Name the blood parasite species.
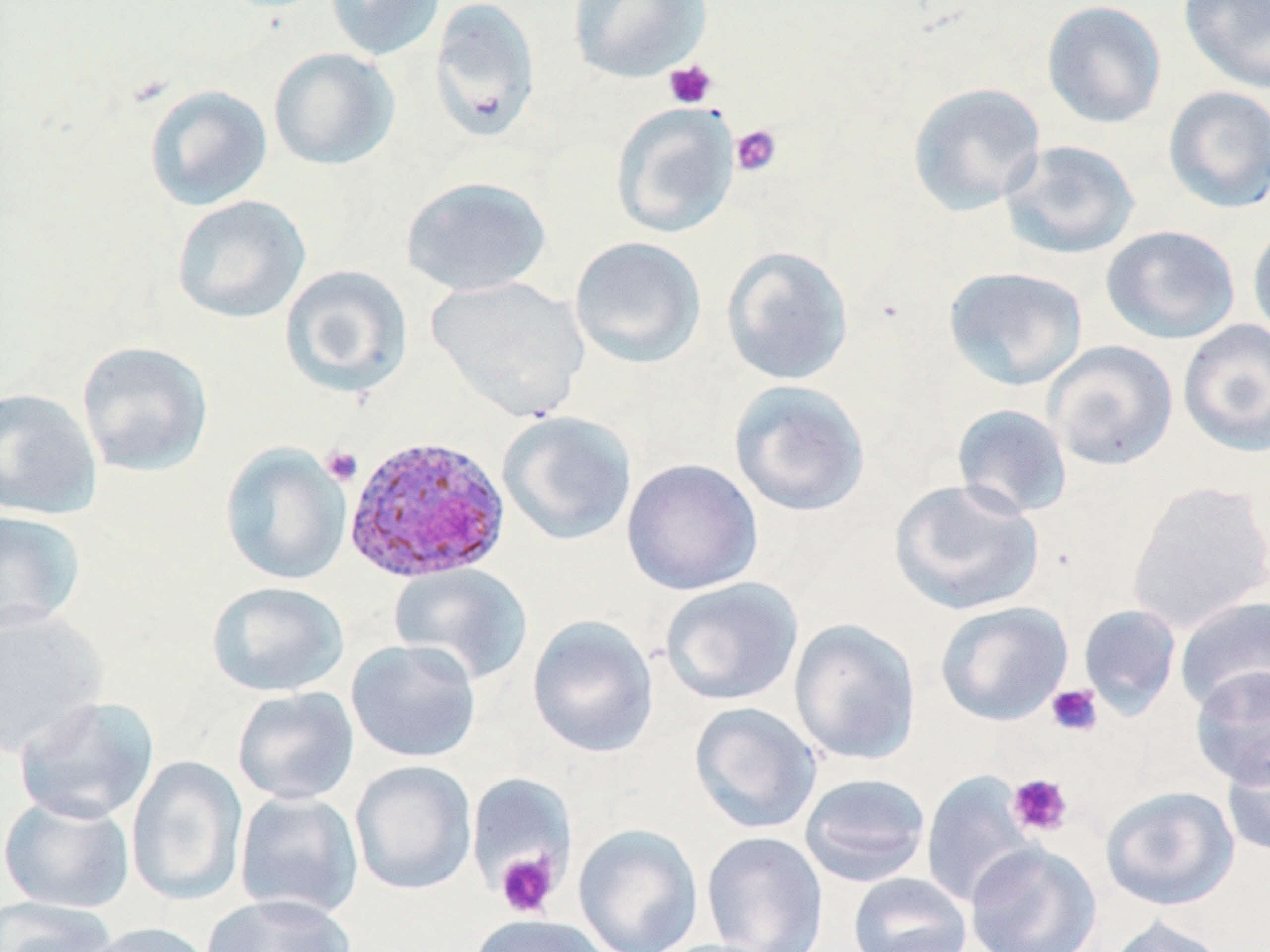

Plasmodium ovale.

magnification = 1000x
stain = May-Grünwald-Giemsa
uninfected red blood cell locations = approximate bounding boxes as (x1,y1)-(x2,y2) corner pairs in pixels: (325,0)-(445,60), (429,0)-(542,141), (569,0)-(711,83), (1041,0)-(1167,129), (1178,0)-(1270,94), (268,47)-(399,170), (907,81)-(1046,216), (143,84)-(273,211), (1162,85)-(1270,214), (611,102)-(740,239), (1000,140)-(1140,260), (400,175)-(552,297), (172,194)-(311,324), (1247,221)-(1270,345), (1101,225)-(1241,345), (569,236)-(707,369), (720,245)-(854,386), (279,264)-(414,398), (943,266)-(1088,391), (427,275)-(589,422), (1177,319)-(1270,457), (75,340)-(214,477), (1044,340)-(1178,471), (728,379)-(871,517), (0,387)-(103,520), (951,404)-(1073,520), (497,410)-(638,547), (220,444)-(351,585), (622,458)-(763,596), (889,478)-(1045,616), (1128,480)-(1270,632), (0,510)-(87,635), (388,564)-(533,684), (659,577)-(804,706), (206,580)-(349,697), (1174,596)-(1270,714), (935,600)-(1073,726), (1078,603)-(1182,718), (0,606)-(109,758), (527,616)-(659,758), (789,618)-(922,766), (346,639)-(482,763), (1190,666)-(1270,790), (231,686)-(360,806), (14,695)-(160,825), (689,701)-(822,834), (1221,743)-(1270,857), (126,755)-(248,906), (350,760)-(477,895), (920,770)-(1038,907), (466,773)-(575,894), (798,773)-(931,887), (1100,785)-(1240,911), (234,792)-(364,921), (0,794)-(135,913), (573,823)-(703,952), (701,831)-(829,952), (964,842)-(1102,952), (847,872)-(973,952), (202,893)-(357,952), (0,896)-(120,952), (469,914)-(613,952), (1105,916)-(1232,952), (81,921)-(217,952)
preparation = thin blood smear
modality = light microscopy
platelet locations = approximate bounding boxes as (x1,y1)-(x2,y2) corner pairs in pixels: (663,60)-(718,109), (730,124)-(782,176), (320,445)-(363,485), (1045,684)-(1103,736), (1007,773)-(1073,837), (495,850)-(559,918)
image size = 1270×952 pixels
Plasmodium ovale-infected red blood cell locations = approximate bounding boxes as (x1,y1)-(x2,y2) corner pairs in pixels: (343,435)-(512,584)
field of view = single